Assess the morphology of the red blood cells.
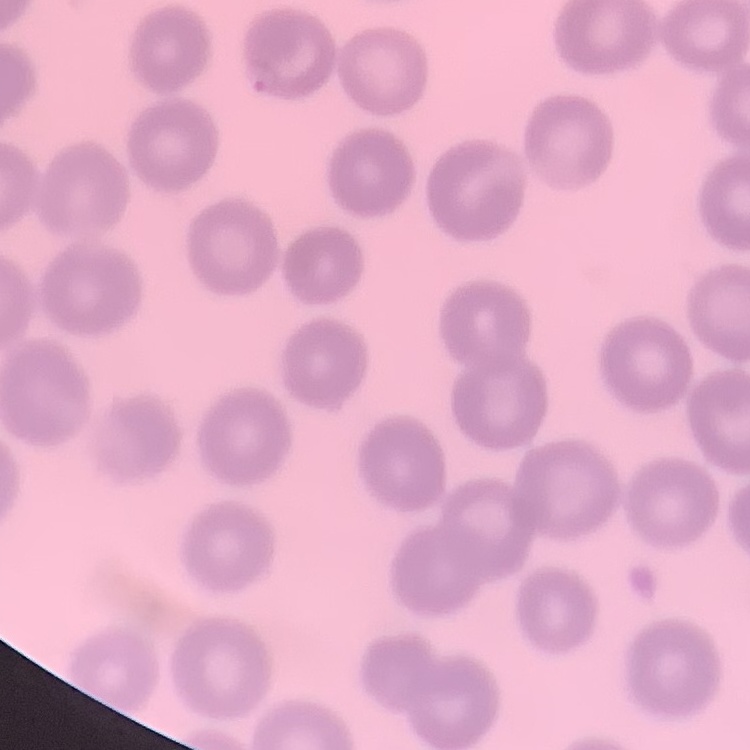

They show no rouleaux formation.

stain: Field's or Giemsa
preparation: thin blood smear
image_type: one tile cut from a larger photomicrograph